Assess this cell for malaria.
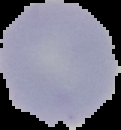
Uninfected.

image size = 121×130 pixels
preparation = thin blood smear
image type = segmented cell region on a black background